Assess this cell for malaria.
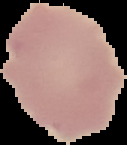
It is uninfected.

preparation = thin blood film
image type = segmented cell region with the area outside set to black
image size = 127×145 pixels